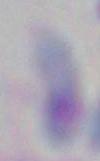

{
  "magnification": "1000x",
  "identification": "Toxoplasma gondii",
  "modality": "photomicrograph"
}